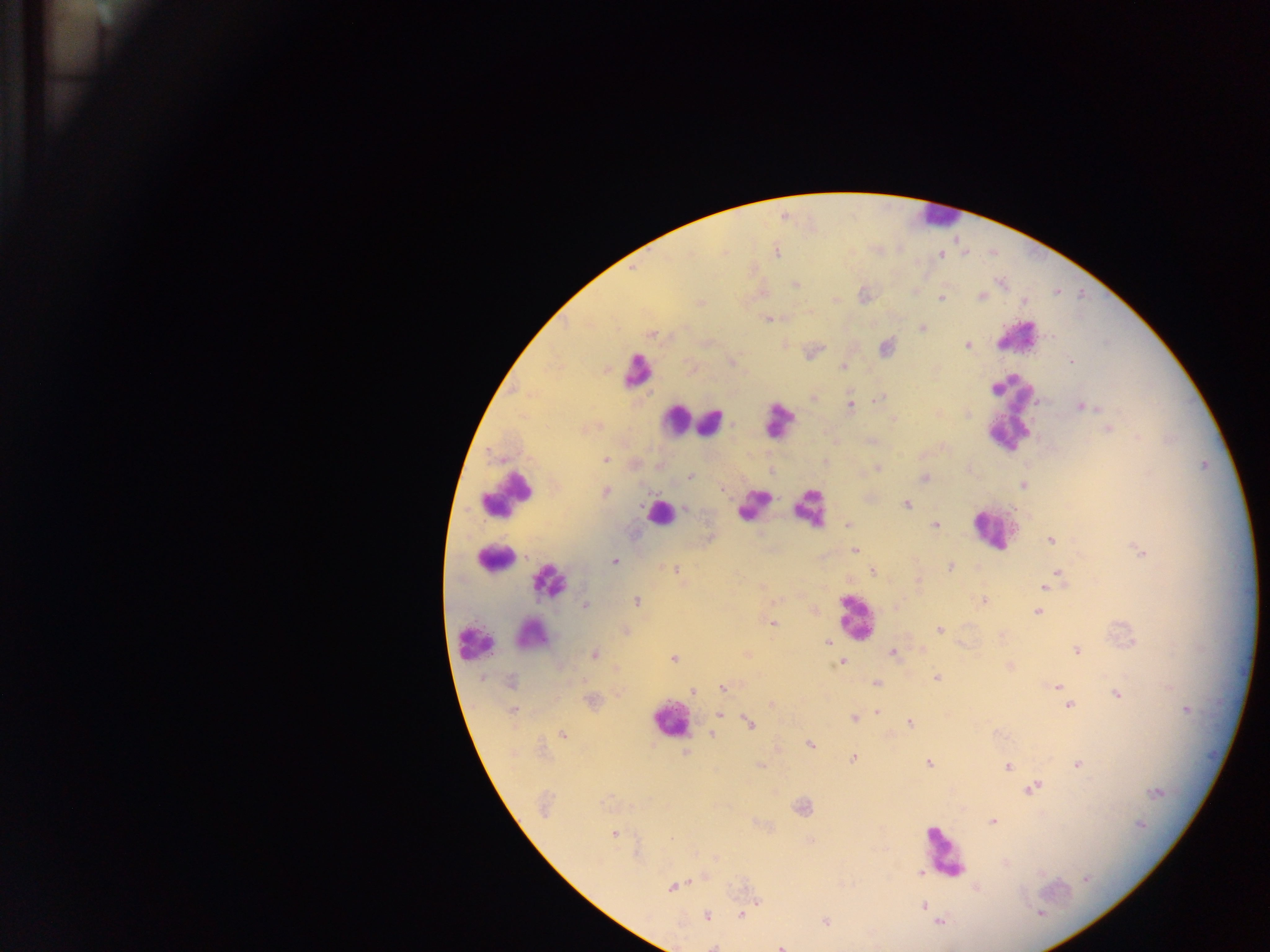

Approximate centers as x y in pixels.
Summary:
  - Malaria parasite locations: 776 253; 941 255; 795 285; 981 296; 941 299; 1024 301; 701 303; 768 318; 923 328; 651 335; 967 345; 886 347; 1071 361; 843 367; 813 397; 880 398; 1038 401; 850 405; 1081 406; 893 419; 1108 428; 1138 438; 605 459; 877 468; 690 477; 924 477; 1022 485; 605 491; 907 505; 685 508; 848 524; 936 525; 1051 540; 855 550; 1140 551; 614 562; 950 566; 676 570; 873 572; 1057 572; 918 581; 1045 586; 984 600; 636 601; 586 606; 1037 612; 773 623; 939 630; 624 631; 828 642; 922 651; 1077 651; 892 653; 594 655; 673 658; 841 662; 1010 666; 937 678; 511 682; 876 683; 1059 687; 723 688; 692 691; 1062 691; 1116 694; 1068 705; 1186 710; 514 711; 876 712; 719 714; 854 718; 749 723; 909 723; 712 733; 562 734; 810 745; 686 753; 853 758; 1078 763; 929 764; 1008 767; 1032 788; 1156 793; 992 822; 1141 825; 614 833; 920 872; 1086 880; 672 888; 923 905; 1040 913; 741 914; 707 916; 825 921; 939 922; 713 947; 780 947
  - Leukocyte locations: 936 216; 1015 335; 637 371; 1008 416; 675 420; 778 420; 711 423; 507 492; 752 505; 809 508; 659 513; 992 528; 493 558; 549 582; 855 616; 532 635; 474 642; 669 721; 944 853
  - Image size: 1270×952 pixels
  - Preparation: thick blood film
  - Capture: mobile-phone photograph through a microscope
  - Field of view: single
  - Country: Ghana